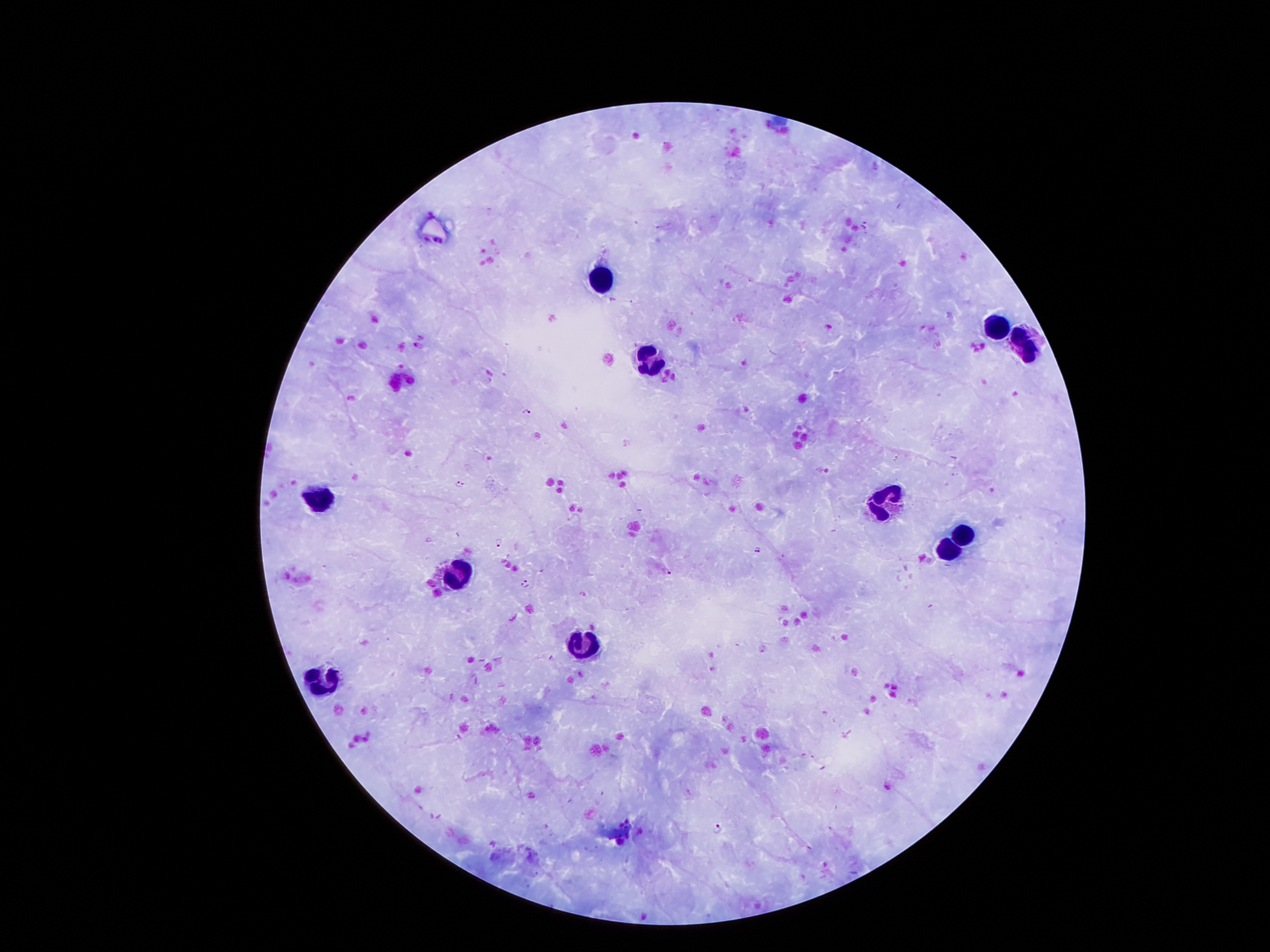
Approximate object centers, in pixels from the top-left corner.
Summary:
  - Leukocyte locations: (x=604, y=276), (x=999, y=327), (x=1016, y=339), (x=649, y=360), (x=315, y=495), (x=886, y=505), (x=961, y=534), (x=949, y=552), (x=455, y=575), (x=583, y=643), (x=323, y=683)
  - Plasmodium parasite locations: (x=866, y=225), (x=526, y=412), (x=459, y=484), (x=498, y=542), (x=759, y=550), (x=666, y=572), (x=526, y=584), (x=805, y=755), (x=888, y=788), (x=532, y=795), (x=718, y=827)
  - Patient malaria status: infected with Plasmodium falciparum
  - Capture: smartphone through the microscope eyepiece
  - Stain: Giemsa
  - Field of view: one from this slide
  - Image size: 1270×952 pixels
  - Preparation: thick peripheral-blood smear
  - Magnification: 100x